Report the malaria status of this cell.
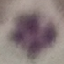

Uninfected.

Automatically extracted cell patch, resized to 64 × 64 pixels. Thin smear of blood. Giemsa stain. Photographed with a smartphone camera at the microscope eyepiece.